Locate every uninfected red blood cell.
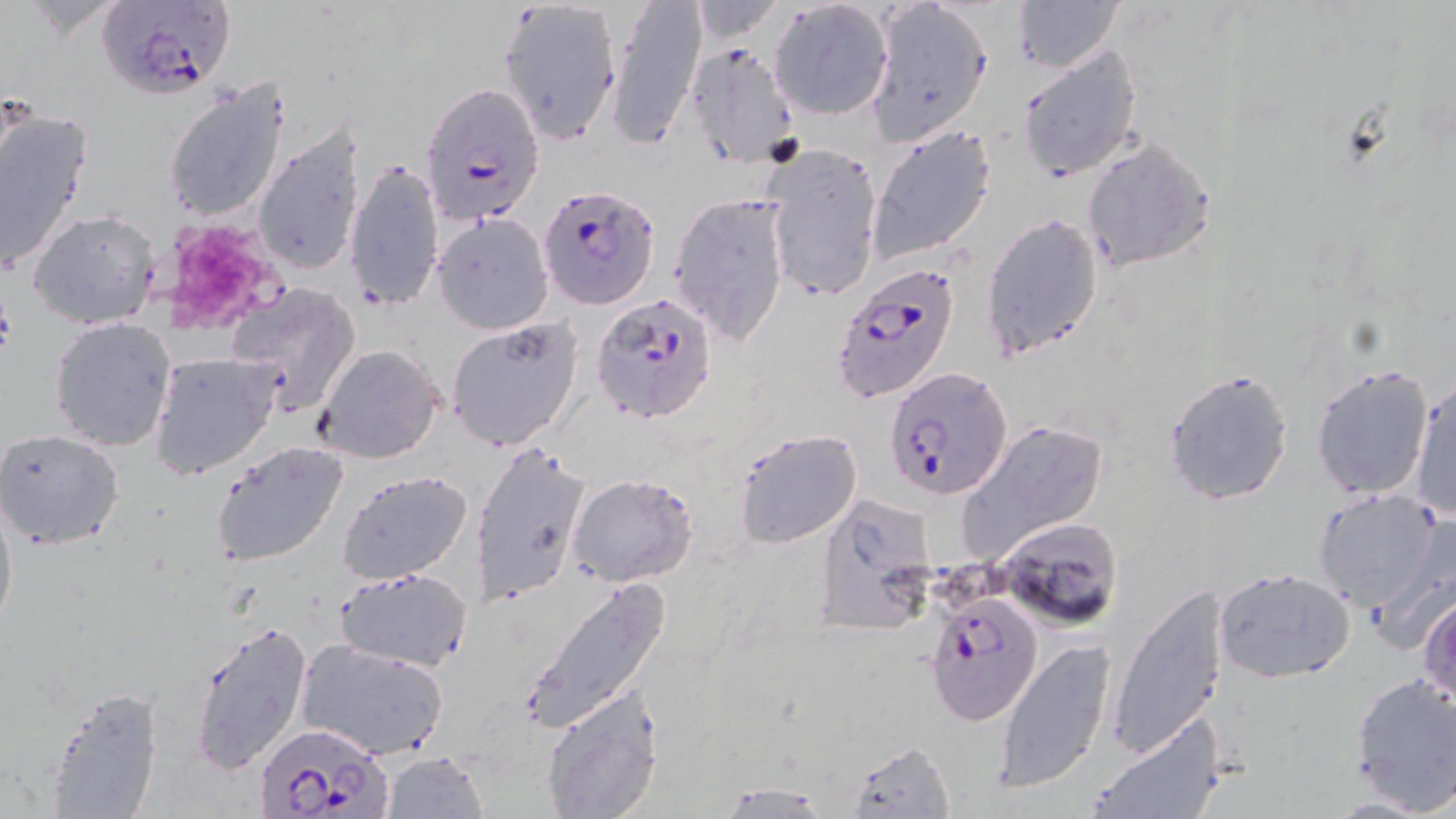
Approximate bounding boxes as [x1, y1, x2, y2] in pixels.
Uninfected red blood cells: [604, 0, 707, 149], [866, 0, 994, 143], [1011, 0, 1122, 70], [496, 1, 623, 144], [769, 3, 894, 121], [684, 40, 799, 167], [1018, 42, 1144, 180], [163, 74, 293, 223], [0, 101, 93, 276], [868, 124, 997, 264], [251, 126, 365, 281], [1081, 136, 1217, 271], [761, 144, 884, 304], [345, 159, 446, 311], [669, 193, 792, 345], [29, 208, 162, 330], [433, 214, 553, 334], [982, 215, 1105, 360], [227, 282, 362, 414], [49, 316, 176, 451], [444, 317, 584, 452], [313, 344, 444, 464], [151, 354, 278, 478], [1309, 364, 1432, 499], [1163, 369, 1296, 507], [1408, 379, 1455, 521], [955, 420, 1109, 560], [1, 428, 125, 551], [733, 428, 862, 549], [209, 440, 350, 569], [474, 440, 592, 608], [339, 453, 593, 598], [336, 469, 477, 585], [567, 473, 697, 588], [0, 489, 17, 639], [1312, 489, 1443, 611], [815, 494, 938, 636], [999, 517, 1124, 630], [334, 566, 474, 671], [1214, 567, 1357, 683], [524, 574, 670, 734], [1108, 583, 1229, 757], [1419, 591, 1456, 709], [185, 616, 315, 776], [297, 638, 449, 759], [992, 639, 1117, 792], [1348, 671, 1456, 812], [39, 684, 166, 819], [541, 690, 664, 818], [1086, 712, 1225, 819], [845, 739, 956, 818], [378, 750, 489, 818], [713, 781, 837, 818].

slide-level diagnosis = Plasmodium falciparum
stain = May-Grünwald-Giemsa
modality = optical microscopy
platelet locations = approximate bounding boxes as [x1, y1, x2, y2] in pixels: [151, 217, 291, 338]
Plasmodium falciparum-infected red blood cell locations = approximate bounding boxes as [x1, y1, x2, y2] in pixels: [100, 0, 235, 100], [421, 82, 545, 223], [539, 184, 660, 309], [836, 262, 961, 402], [592, 293, 719, 428], [884, 368, 1013, 501], [925, 591, 1044, 726], [254, 722, 390, 817]
image size = 1456×819 pixels
magnification = 1000x
field of view = single
preparation = thin blood smear